Outline each uninfected red blood cell.
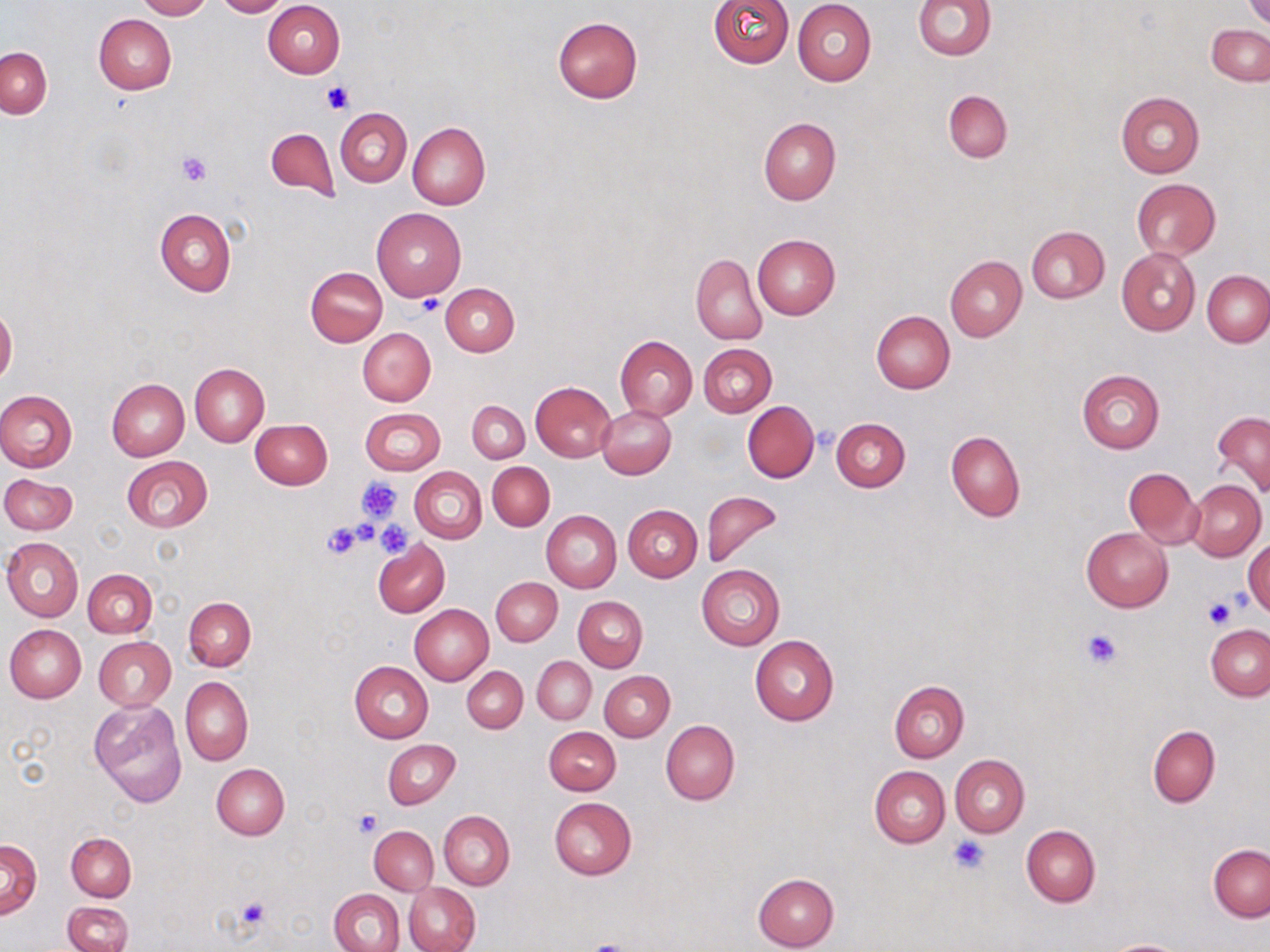
Approximate bounding boxes as named x1/y1/x2/y2 corners in pixels.
Uninfected red blood cells: (x1=136, y1=0, x2=212, y2=20), (x1=215, y1=0, x2=287, y2=17), (x1=707, y1=0, x2=794, y2=67), (x1=913, y1=0, x2=996, y2=60), (x1=263, y1=1, x2=344, y2=78), (x1=792, y1=1, x2=877, y2=86), (x1=1245, y1=1, x2=1270, y2=27), (x1=93, y1=14, x2=177, y2=94), (x1=552, y1=17, x2=644, y2=103), (x1=1207, y1=25, x2=1270, y2=85), (x1=0, y1=47, x2=51, y2=118), (x1=943, y1=89, x2=1012, y2=162), (x1=1114, y1=91, x2=1205, y2=178), (x1=336, y1=108, x2=412, y2=187), (x1=758, y1=117, x2=840, y2=205), (x1=407, y1=122, x2=490, y2=210), (x1=265, y1=128, x2=339, y2=201), (x1=1132, y1=179, x2=1221, y2=259), (x1=156, y1=207, x2=235, y2=296), (x1=372, y1=207, x2=466, y2=301), (x1=1027, y1=226, x2=1109, y2=303), (x1=753, y1=235, x2=840, y2=319), (x1=1116, y1=247, x2=1202, y2=337), (x1=690, y1=254, x2=767, y2=344), (x1=945, y1=256, x2=1026, y2=341), (x1=306, y1=267, x2=387, y2=346), (x1=1202, y1=271, x2=1270, y2=347), (x1=441, y1=283, x2=520, y2=357), (x1=1, y1=306, x2=17, y2=386), (x1=871, y1=311, x2=955, y2=394), (x1=358, y1=328, x2=435, y2=405), (x1=614, y1=335, x2=697, y2=419), (x1=698, y1=343, x2=777, y2=417), (x1=190, y1=363, x2=269, y2=446), (x1=1077, y1=368, x2=1165, y2=454), (x1=106, y1=378, x2=189, y2=461), (x1=530, y1=381, x2=617, y2=463), (x1=0, y1=389, x2=78, y2=473), (x1=466, y1=401, x2=529, y2=463), (x1=743, y1=402, x2=819, y2=482), (x1=597, y1=406, x2=676, y2=478), (x1=360, y1=407, x2=445, y2=475), (x1=1212, y1=410, x2=1270, y2=496), (x1=831, y1=417, x2=911, y2=492), (x1=249, y1=419, x2=332, y2=489), (x1=945, y1=432, x2=1025, y2=522), (x1=121, y1=456, x2=212, y2=532), (x1=488, y1=462, x2=555, y2=531), (x1=411, y1=468, x2=486, y2=542), (x1=1123, y1=468, x2=1203, y2=548), (x1=1, y1=474, x2=78, y2=534), (x1=1188, y1=480, x2=1265, y2=560), (x1=701, y1=489, x2=784, y2=569), (x1=623, y1=505, x2=702, y2=581), (x1=541, y1=511, x2=621, y2=592), (x1=1081, y1=527, x2=1173, y2=612), (x1=2, y1=537, x2=83, y2=622), (x1=1245, y1=539, x2=1269, y2=618), (x1=373, y1=541, x2=449, y2=618), (x1=696, y1=564, x2=785, y2=650), (x1=83, y1=569, x2=157, y2=638), (x1=491, y1=577, x2=563, y2=646), (x1=574, y1=596, x2=647, y2=672), (x1=184, y1=597, x2=255, y2=670), (x1=409, y1=604, x2=494, y2=685), (x1=4, y1=624, x2=86, y2=702), (x1=1206, y1=625, x2=1270, y2=700), (x1=750, y1=635, x2=839, y2=725), (x1=93, y1=636, x2=176, y2=711), (x1=532, y1=656, x2=596, y2=725), (x1=350, y1=661, x2=433, y2=742), (x1=462, y1=666, x2=528, y2=732), (x1=600, y1=671, x2=674, y2=741), (x1=180, y1=676, x2=253, y2=765), (x1=889, y1=680, x2=970, y2=762), (x1=89, y1=700, x2=188, y2=808), (x1=661, y1=720, x2=739, y2=805), (x1=1147, y1=725, x2=1220, y2=808), (x1=544, y1=726, x2=620, y2=795), (x1=383, y1=740, x2=460, y2=809), (x1=950, y1=755, x2=1029, y2=838), (x1=211, y1=763, x2=289, y2=840), (x1=869, y1=765, x2=950, y2=847), (x1=549, y1=796, x2=636, y2=879), (x1=439, y1=810, x2=515, y2=889), (x1=1021, y1=825, x2=1100, y2=907), (x1=369, y1=826, x2=438, y2=895), (x1=66, y1=832, x2=136, y2=901), (x1=1, y1=840, x2=41, y2=917), (x1=1208, y1=844, x2=1270, y2=921), (x1=752, y1=873, x2=840, y2=951), (x1=404, y1=882, x2=480, y2=952), (x1=330, y1=888, x2=404, y2=952), (x1=63, y1=902, x2=134, y2=952), (x1=1102, y1=939, x2=1191, y2=952).

Platelet locations: (x1=321, y1=79, x2=354, y2=115), (x1=177, y1=151, x2=212, y2=187), (x1=416, y1=296, x2=444, y2=316), (x1=814, y1=425, x2=838, y2=450), (x1=356, y1=476, x2=403, y2=521), (x1=375, y1=519, x2=412, y2=557), (x1=322, y1=522, x2=364, y2=559), (x1=1202, y1=596, x2=1237, y2=630), (x1=1081, y1=629, x2=1121, y2=668), (x1=352, y1=808, x2=383, y2=837), (x1=948, y1=834, x2=989, y2=873), (x1=234, y1=898, x2=271, y2=931), (x1=580, y1=940, x2=638, y2=952). Slide-level diagnosis: negative for blood parasites. May-Grünwald-Giemsa-stained preparation. Thin blood film. Optical microscopy. Image is 1270×952 pixels. 1000x magnification. Single field of view.